Identify the blood parasite species.
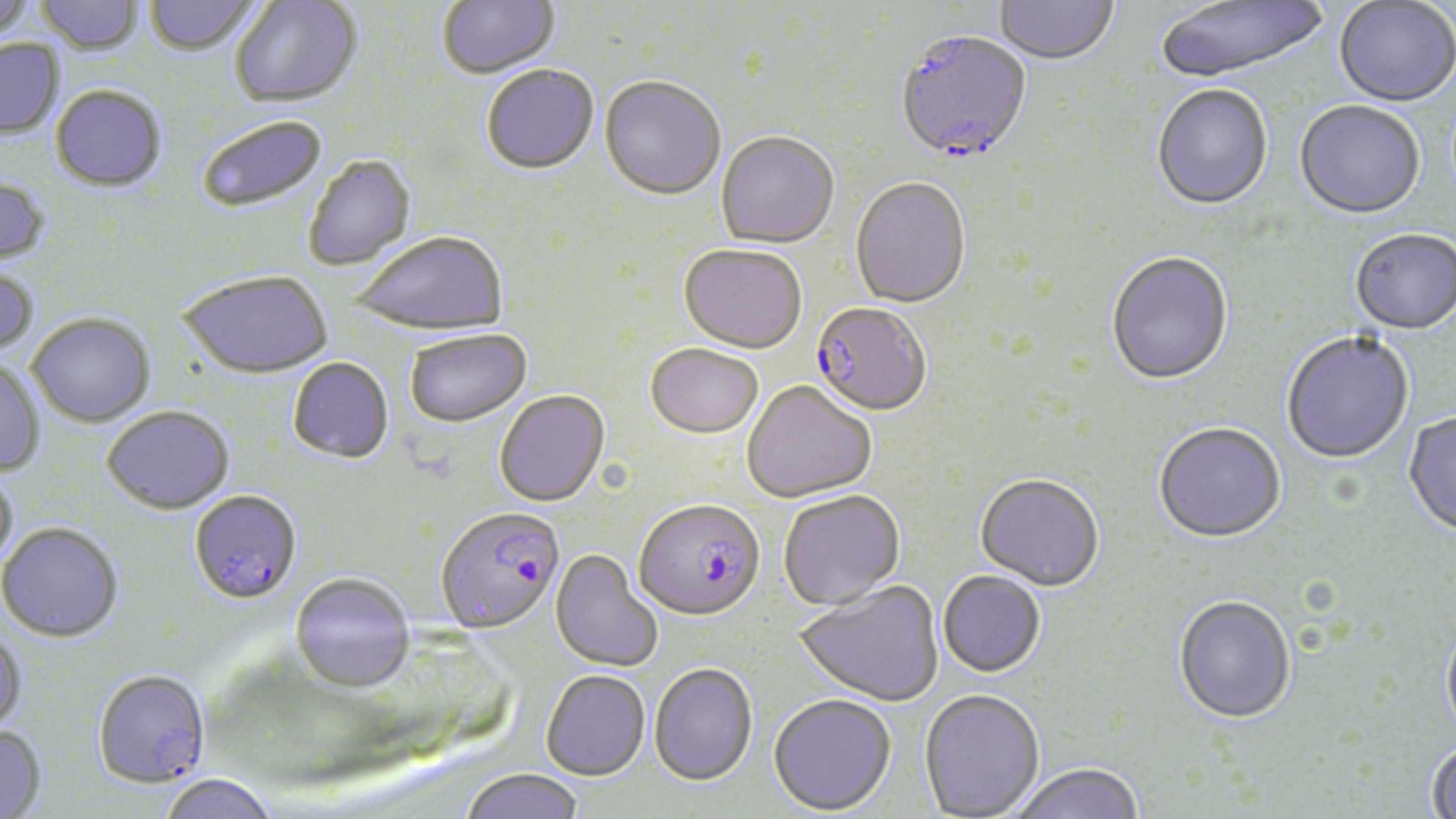
Plasmodium falciparum.

Approximate bounding boxes as [x1, y1, x2, y2] in pixels. Uninfected red blood cell locations: [0, 0, 36, 42], [36, 0, 143, 57], [144, 0, 262, 58], [230, 0, 362, 111], [438, 0, 559, 81], [994, 0, 1118, 68], [1155, 0, 1330, 85], [1333, 1, 1456, 109], [0, 40, 64, 140], [482, 66, 599, 177], [599, 78, 725, 202], [1152, 86, 1273, 212], [50, 87, 167, 194], [1294, 102, 1425, 222], [197, 117, 328, 214], [716, 133, 839, 250], [303, 156, 417, 273], [0, 175, 51, 268], [850, 179, 971, 311], [1350, 231, 1456, 337], [353, 234, 507, 339], [678, 246, 807, 356], [1106, 253, 1233, 388], [0, 266, 39, 358], [179, 273, 333, 382], [27, 315, 155, 429], [405, 331, 532, 430], [1281, 333, 1414, 465], [645, 345, 763, 442], [287, 358, 394, 465], [0, 359, 46, 477], [742, 382, 877, 504], [494, 391, 611, 509], [102, 407, 234, 517], [1403, 413, 1456, 539], [1153, 425, 1286, 546], [0, 469, 19, 572], [975, 476, 1104, 593], [778, 491, 906, 613], [0, 524, 123, 645], [550, 550, 663, 673], [937, 572, 1046, 679], [290, 575, 415, 696], [794, 580, 944, 708], [1173, 597, 1296, 725], [1440, 621, 1456, 744], [0, 628, 27, 735], [649, 664, 758, 788], [540, 670, 650, 781], [919, 691, 1045, 819], [768, 695, 897, 817], [0, 726, 47, 819], [1425, 740, 1456, 818], [1012, 764, 1144, 819], [461, 769, 584, 819], [160, 776, 276, 819]. Plasmodium falciparum-infected red blood cell locations: [896, 34, 1033, 167], [809, 304, 932, 419], [189, 491, 302, 607], [634, 501, 765, 624], [436, 509, 564, 636], [92, 672, 210, 791]. May-Grünwald-Giemsa-stained preparation. One field of a larger specimen. Image is 1456×819 pixels. 1000x magnification. Optical microscopy. Thin blood smear.